Assess this cell for malaria.
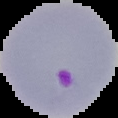

Parasitized.

image_size: 118×118 pixels
preparation: thin blood film
image_type: segmented cell region on a black background